Mark where platelets are.
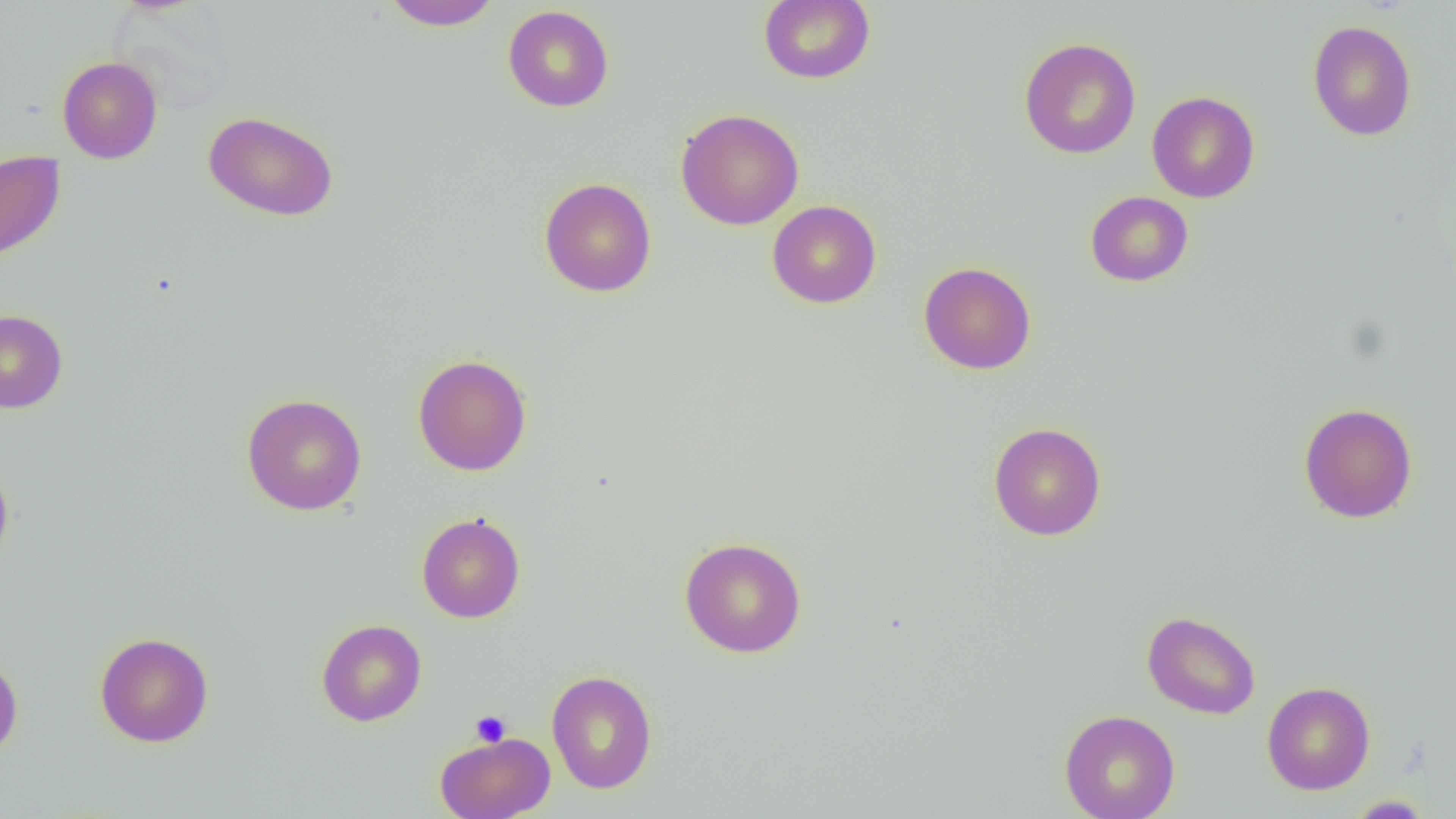

Approximate bounding boxes as [x1, y1, x2, y2] in pixels.
Platelets: [471, 710, 511, 747].

slide-level diagnosis = no evidence of blood parasites
uninfected red blood cell locations = approximate bounding boxes as [x1, y1, x2, y2] in pixels: [380, 0, 501, 30], [758, 0, 875, 85], [503, 5, 614, 112], [1307, 20, 1417, 141], [1019, 37, 1141, 159], [57, 56, 162, 164], [1147, 91, 1260, 203], [676, 108, 804, 230], [203, 110, 339, 222], [0, 151, 66, 264], [539, 177, 657, 297], [1085, 191, 1194, 287], [767, 200, 882, 308], [918, 262, 1036, 375], [0, 310, 68, 413], [412, 354, 532, 476], [241, 393, 367, 515], [1298, 402, 1418, 524], [988, 422, 1106, 541], [0, 457, 14, 569], [416, 512, 525, 623], [679, 536, 806, 658], [1141, 611, 1261, 719], [316, 619, 427, 726], [94, 632, 214, 747], [0, 653, 23, 762], [546, 669, 658, 793], [1262, 681, 1375, 795], [1059, 709, 1180, 819], [435, 731, 555, 819], [1344, 795, 1434, 818]
modality = optical microscopy
magnification = 1000x
field of view = single
preparation = thin blood film
image size = 1456×819 pixels